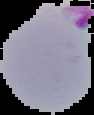

result = Plasmodium parasites identified
image type = segmented cell region with the area outside set to black
image size = 94×115 pixels
preparation = thin blood smear